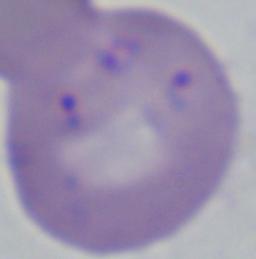
modality = micrograph
identification = Babesia
magnification = 1000x